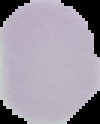

image type = cell region segmented out of the field of view; surrounding area masked to black
malaria status = uninfected
preparation = thin blood film
image size = 100×124 pixels